Describe the morphology of the erythrocytes.
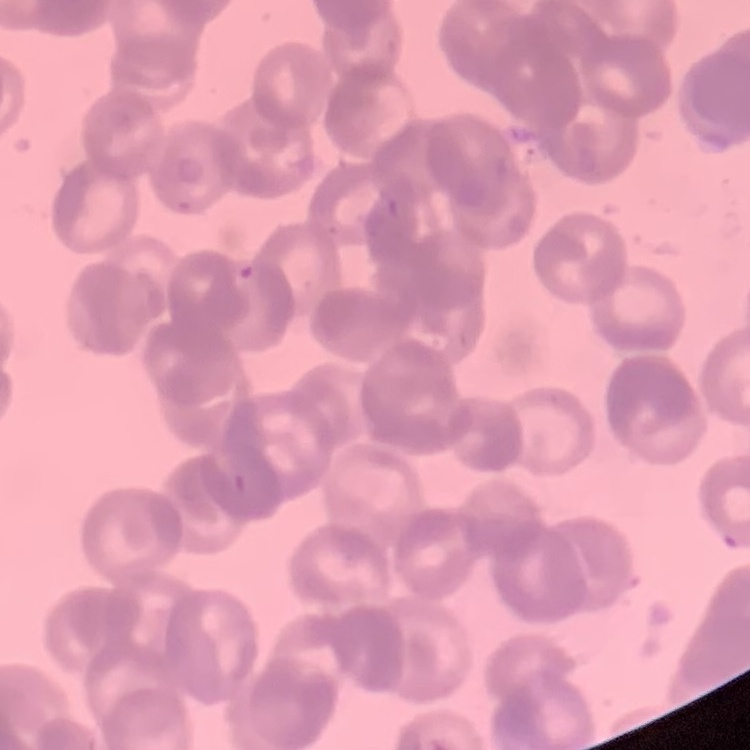
Rouleaux formation.

preparation = thin blood film
image type = square crop of a larger photomicrograph
stain = Field's or Giemsa